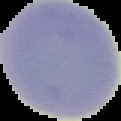

preparation = thin blood film
image type = segmented cell region on a black background
image size = 121×121 pixels
result = negative for Plasmodium parasites